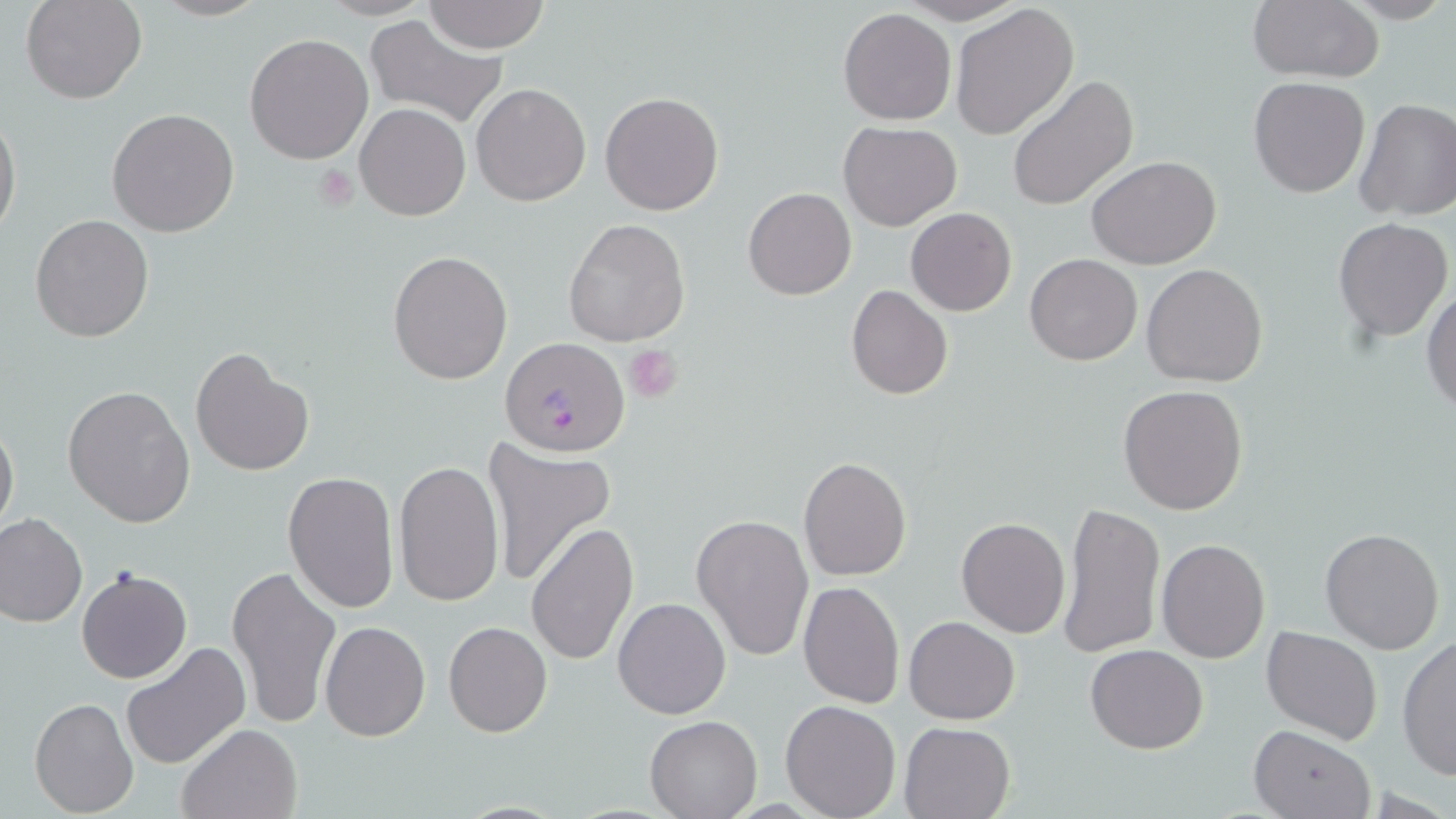

slide-level diagnosis = Plasmodium falciparum
magnification = 1000x
uninfected red blood cell locations = approximate bounding boxes as [x1, y1, x2, y2] in pixels: [21, 0, 146, 104], [147, 0, 270, 22], [425, 0, 549, 53], [897, 0, 1028, 25], [1248, 0, 1387, 83], [949, 4, 1079, 141], [839, 8, 957, 126], [363, 14, 508, 130], [244, 33, 374, 163], [1006, 75, 1138, 213], [1249, 77, 1370, 198], [471, 82, 592, 207], [600, 91, 725, 215], [1356, 98, 1456, 222], [354, 102, 470, 221], [106, 108, 240, 238], [1, 110, 22, 241], [839, 122, 963, 231], [1087, 156, 1223, 270], [743, 187, 856, 300], [905, 208, 1016, 316], [30, 214, 156, 342], [1333, 216, 1452, 342], [564, 218, 691, 347], [387, 249, 513, 384], [1025, 253, 1143, 366], [1141, 262, 1269, 388], [1422, 284, 1456, 416], [846, 285, 952, 400], [189, 346, 313, 477], [1118, 383, 1249, 514], [63, 384, 195, 527], [0, 418, 19, 542], [482, 438, 617, 589], [798, 457, 911, 581], [392, 461, 504, 606], [283, 471, 399, 616], [1057, 502, 1164, 662], [0, 512, 87, 627], [691, 513, 814, 661], [956, 517, 1071, 638], [525, 523, 638, 666], [1320, 527, 1446, 655], [1156, 538, 1269, 662], [226, 564, 341, 731], [76, 568, 191, 684], [797, 582, 905, 707], [612, 597, 731, 720], [903, 615, 1021, 724], [320, 620, 430, 740], [443, 621, 553, 737], [1261, 626, 1384, 746], [1397, 636, 1455, 779], [119, 641, 252, 771], [1085, 643, 1208, 754], [29, 697, 137, 817], [781, 698, 901, 819], [645, 714, 761, 818], [898, 720, 1017, 818], [176, 722, 303, 819], [1249, 726, 1376, 819]
preparation = thin blood film
modality = optical microscopy
field of view = one of a larger specimen
image size = 1456×819 pixels
platelet locations = approximate bounding boxes as [x1, y1, x2, y2] in pixels: [314, 166, 357, 210], [624, 344, 683, 403]
Plasmodium falciparum-infected red blood cell locations = approximate bounding boxes as [x1, y1, x2, y2] in pixels: [501, 341, 632, 455]
stain = May-Grünwald-Giemsa